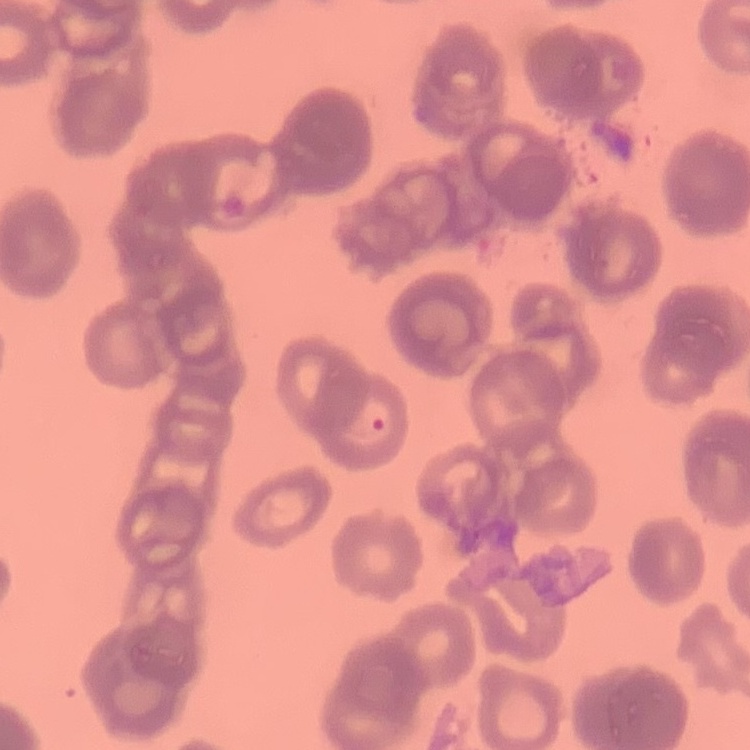

erythrocyte morphology = rouleaux formation
preparation = thin blood film
image type = one tile cut from a larger photomicrograph
stain = Field's or Giemsa